Point out each malaria parasite.
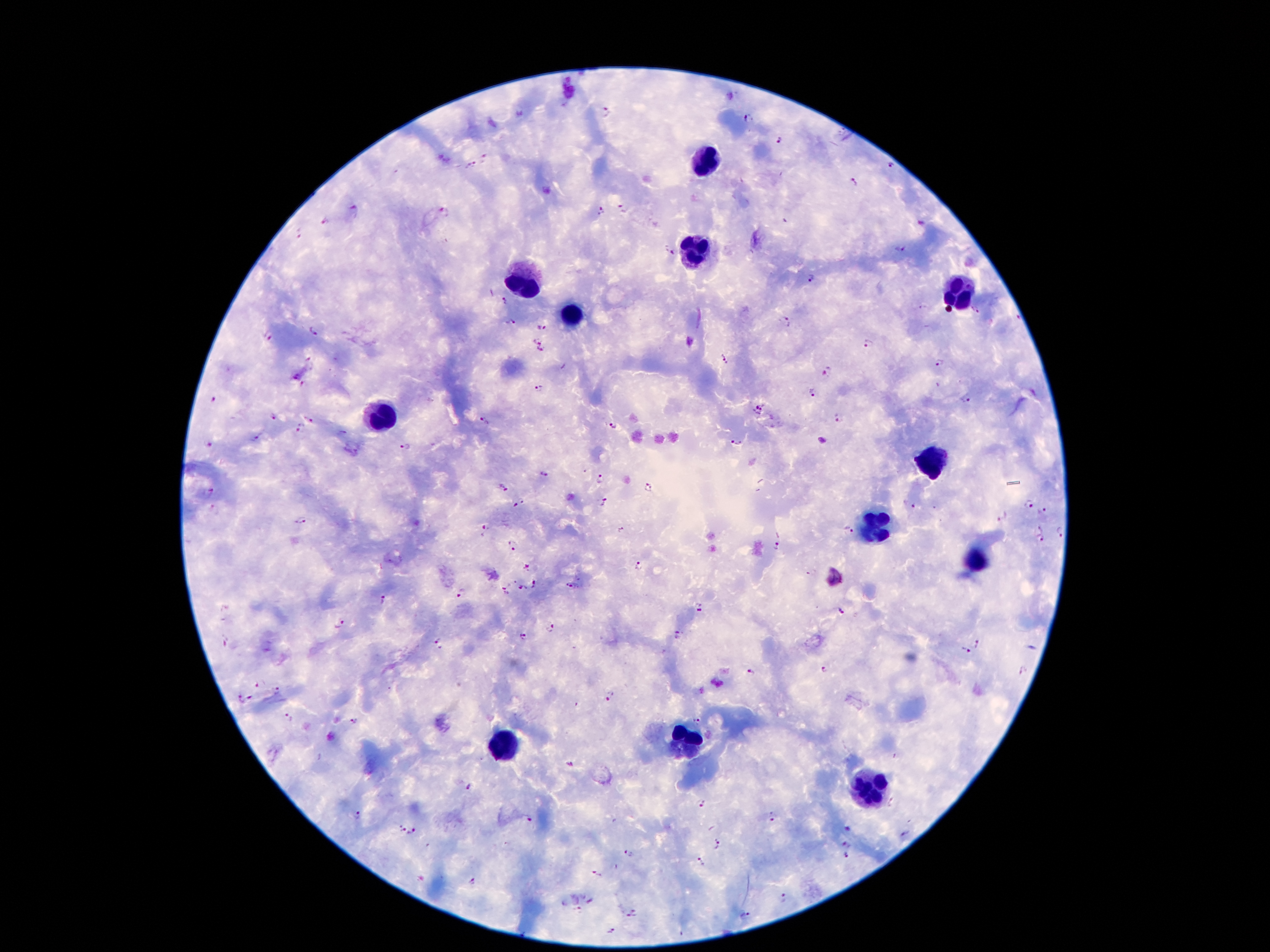

Approximate centers as (x, y) in pixels.
Malaria parasites: (604, 111), (748, 120), (779, 141), (486, 159), (473, 164), (890, 166), (852, 183), (352, 209), (623, 209), (601, 211), (444, 212), (326, 221), (919, 225), (298, 234), (901, 250), (668, 252), (810, 280), (504, 300), (923, 308), (975, 313), (509, 322), (784, 322), (541, 327), (314, 331), (267, 337), (537, 340), (865, 342), (540, 352), (725, 358), (938, 364), (828, 372), (539, 388), (811, 393), (214, 400), (965, 400), (759, 409), (274, 417), (309, 417), (838, 418), (482, 421), (613, 425), (301, 428), (254, 439), (209, 444), (735, 445), (405, 447), (545, 473), (600, 479), (648, 486), (503, 489), (211, 490), (519, 502), (604, 503), (1028, 506), (909, 507), (214, 510), (1043, 512), (1002, 518), (302, 521), (484, 528), (620, 530), (1037, 530), (848, 531), (1060, 532), (1041, 541), (513, 545), (777, 547), (638, 565), (527, 567), (537, 585), (570, 586), (523, 590), (506, 591), (460, 593), (382, 601), (699, 608), (841, 611), (340, 622), (552, 630), (524, 635), (678, 635), (225, 641), (439, 643), (978, 644), (965, 651), (824, 670), (750, 672), (258, 683), (277, 690), (610, 697), (249, 698), (240, 699), (287, 718), (353, 722), (697, 722), (569, 764), (466, 785), (700, 803), (358, 814), (771, 817), (529, 821), (401, 829), (848, 829), (413, 832), (903, 836), (845, 844), (716, 845), (629, 854), (846, 857), (699, 863), (596, 874), (473, 882), (783, 899), (591, 902), (578, 910), (633, 915), (744, 916), (611, 931).

Leukocyte locations: (709, 160), (695, 251), (526, 284), (955, 295), (573, 314), (380, 419), (934, 461), (879, 526), (976, 560), (501, 742), (682, 747), (873, 789). One field from this slide. Photographed through the microscope eyepiece with a smartphone camera. 100x magnification. Thick blood film. Giemsa stain. Image is 1270×952 pixels. Patient malaria status: infected with Plasmodium falciparum.